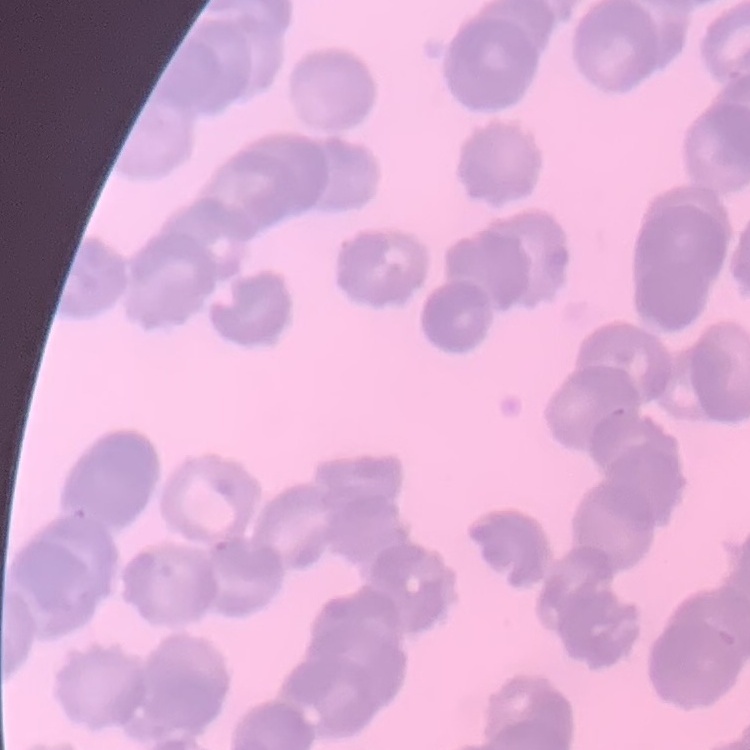
Summary:
  - Red blood cell morphology: rouleaux formation
  - Stain: Field's or Giemsa
  - Image type: one tile cut from a larger photomicrograph
  - Preparation: thin blood film